Locate every Plasmodium falciparum-infected red blood cell.
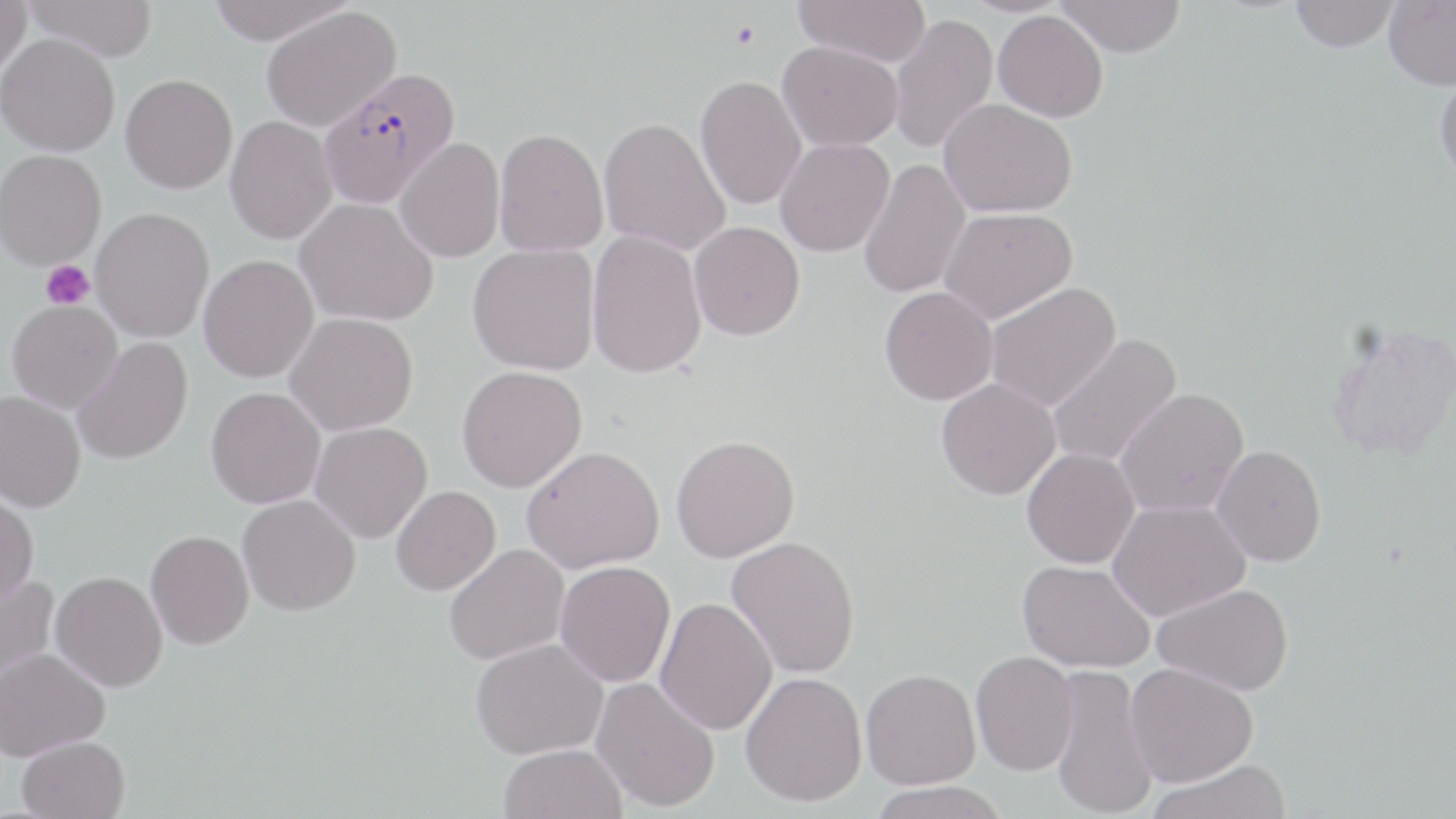
Approximate bounding boxes as [x1, y1, x2, y2] in pixels.
Plasmodium falciparum-infected red blood cells: [318, 67, 460, 209].

slide-level diagnosis = Plasmodium falciparum
modality = optical microscopy
magnification = 1000x
stain = May-Grünwald-Giemsa
field of view = one of a larger specimen
uninfected red blood cell locations = approximate bounding boxes as [x1, y1, x2, y2] in pixels: [0, 0, 31, 80], [23, 0, 158, 62], [205, 0, 354, 44], [793, 0, 930, 68], [1057, 0, 1186, 57], [1290, 0, 1398, 52], [1382, 0, 1456, 92], [261, 6, 401, 132], [993, 10, 1108, 122], [888, 13, 998, 154], [0, 32, 120, 156], [777, 41, 903, 151], [1434, 72, 1456, 188], [120, 74, 237, 193], [695, 75, 807, 210], [938, 99, 1078, 217], [225, 115, 337, 244], [598, 117, 730, 255], [494, 128, 608, 256], [394, 137, 505, 263], [775, 138, 894, 257], [0, 149, 106, 269], [858, 158, 971, 299], [295, 198, 438, 326], [90, 207, 214, 342], [938, 207, 1077, 323], [689, 221, 805, 340], [586, 230, 707, 379], [467, 244, 601, 374], [199, 255, 319, 382], [984, 281, 1121, 413], [879, 286, 998, 405], [7, 300, 122, 412], [285, 313, 418, 435], [1324, 320, 1456, 462], [1047, 333, 1182, 469], [73, 337, 192, 465], [456, 365, 587, 493], [936, 378, 1060, 500], [206, 387, 325, 508], [1115, 387, 1249, 517], [0, 391, 86, 512], [310, 422, 432, 543], [671, 434, 799, 562], [522, 445, 664, 574], [1211, 445, 1326, 566], [1022, 448, 1140, 568], [391, 486, 500, 595], [0, 488, 39, 608], [238, 495, 361, 616], [1108, 498, 1250, 621], [146, 530, 254, 649], [727, 535, 860, 678], [444, 544, 569, 665], [555, 560, 675, 687], [1018, 560, 1154, 673], [50, 571, 168, 691], [0, 575, 58, 697], [1152, 583, 1294, 696], [655, 597, 777, 735], [471, 638, 607, 759], [1, 647, 109, 760], [971, 650, 1079, 775], [1126, 662, 1258, 786], [1050, 664, 1158, 819], [861, 668, 981, 789], [741, 671, 867, 806], [591, 677, 720, 811], [17, 735, 130, 819], [499, 743, 627, 819], [1149, 757, 1291, 819], [867, 781, 1012, 819]
image size = 1456×819 pixels
platelet locations = approximate bounding boxes as [x1, y1, x2, y2] in pixels: [40, 260, 94, 310]
preparation = thin blood film